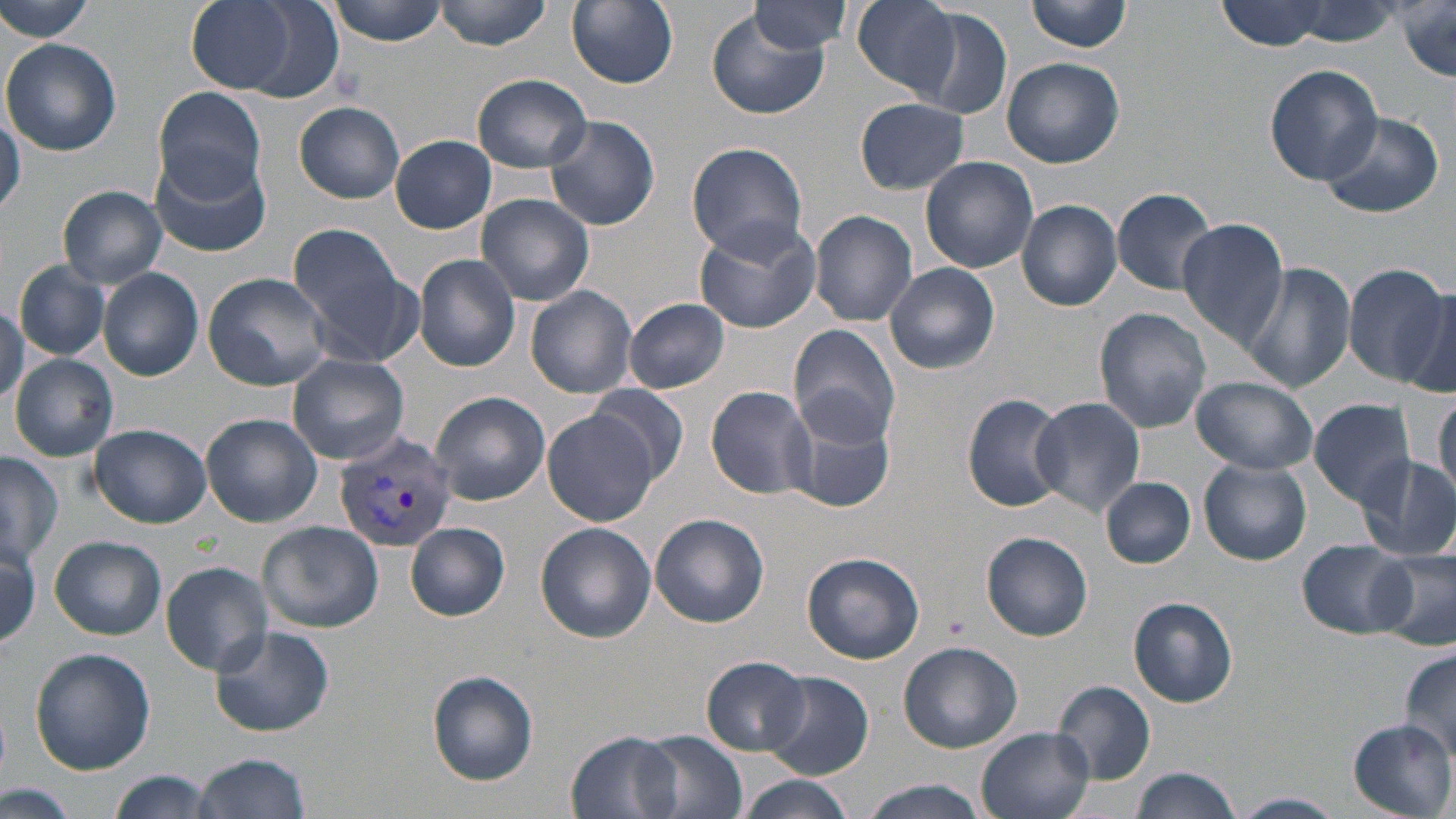

Approximate bounding boxes as (x1,y1)-(x2,y2) corner pairs in pixels. Uninfected red blood cell locations: (185,0)-(341,103), (323,0)-(448,44), (436,0)-(553,50), (567,0)-(678,88), (1025,0)-(1134,53), (0,1)-(96,43), (852,1)-(961,100), (1213,1)-(1357,52), (749,2)-(851,54), (1394,2)-(1456,84), (909,7)-(1012,118), (705,9)-(832,120), (2,36)-(123,157), (1002,56)-(1125,168), (1264,64)-(1384,186), (472,74)-(593,173), (153,84)-(267,200), (855,97)-(970,194), (295,102)-(404,203), (0,108)-(22,218), (1318,111)-(1441,218), (545,115)-(660,231), (390,134)-(497,234), (687,142)-(809,259), (151,147)-(273,258), (920,155)-(1037,274), (1112,185)-(1220,295), (59,186)-(168,288), (475,194)-(593,306), (1018,199)-(1122,311), (807,210)-(918,327), (1176,216)-(1288,350), (692,217)-(824,334), (287,223)-(420,365), (414,254)-(521,373), (1241,260)-(1355,395), (16,262)-(110,360), (885,262)-(999,375), (1344,262)-(1450,385), (98,268)-(204,381), (202,272)-(335,391), (1393,283)-(1456,400), (526,286)-(639,398), (624,298)-(730,394), (1093,307)-(1211,433), (788,324)-(905,447), (9,354)-(118,462), (288,354)-(410,464), (1191,375)-(1317,475), (588,382)-(689,483), (705,385)-(817,500), (1431,388)-(1456,504), (429,391)-(550,504), (960,391)-(1066,511), (1030,395)-(1145,518), (1307,398)-(1420,507), (782,400)-(898,516), (542,410)-(663,527), (201,413)-(324,529), (89,423)-(211,528), (0,451)-(62,563), (1355,455)-(1456,560), (1199,459)-(1312,565), (1101,477)-(1194,568), (650,512)-(769,627), (256,521)-(385,635), (534,522)-(657,643), (406,523)-(509,621), (982,532)-(1093,641), (50,536)-(166,639), (1297,539)-(1416,639), (1,540)-(42,650), (1373,548)-(1456,649), (803,551)-(925,664), (162,560)-(273,674), (1129,597)-(1238,707), (209,625)-(334,737), (898,642)-(1023,752), (29,647)-(156,775), (1399,650)-(1456,764), (701,657)-(810,755), (427,669)-(539,785), (761,670)-(875,779), (1052,681)-(1156,784), (1349,719)-(1455,816), (977,728)-(1095,819), (566,731)-(685,818), (635,732)-(749,817), (193,752)-(314,819), (1128,767)-(1240,819), (105,771)-(220,818), (733,777)-(855,819), (858,778)-(991,819), (5,784)-(79,819), (1230,794)-(1343,819). Plasmodium vivax-infected red blood cell locations: (333,433)-(457,554). Slide-level diagnosis: Plasmodium vivax. Thin blood film. Optical microscopy. 1000x magnification. One field of a larger specimen. Image is 1456×819 pixels. May-Grünwald-Giemsa stain.